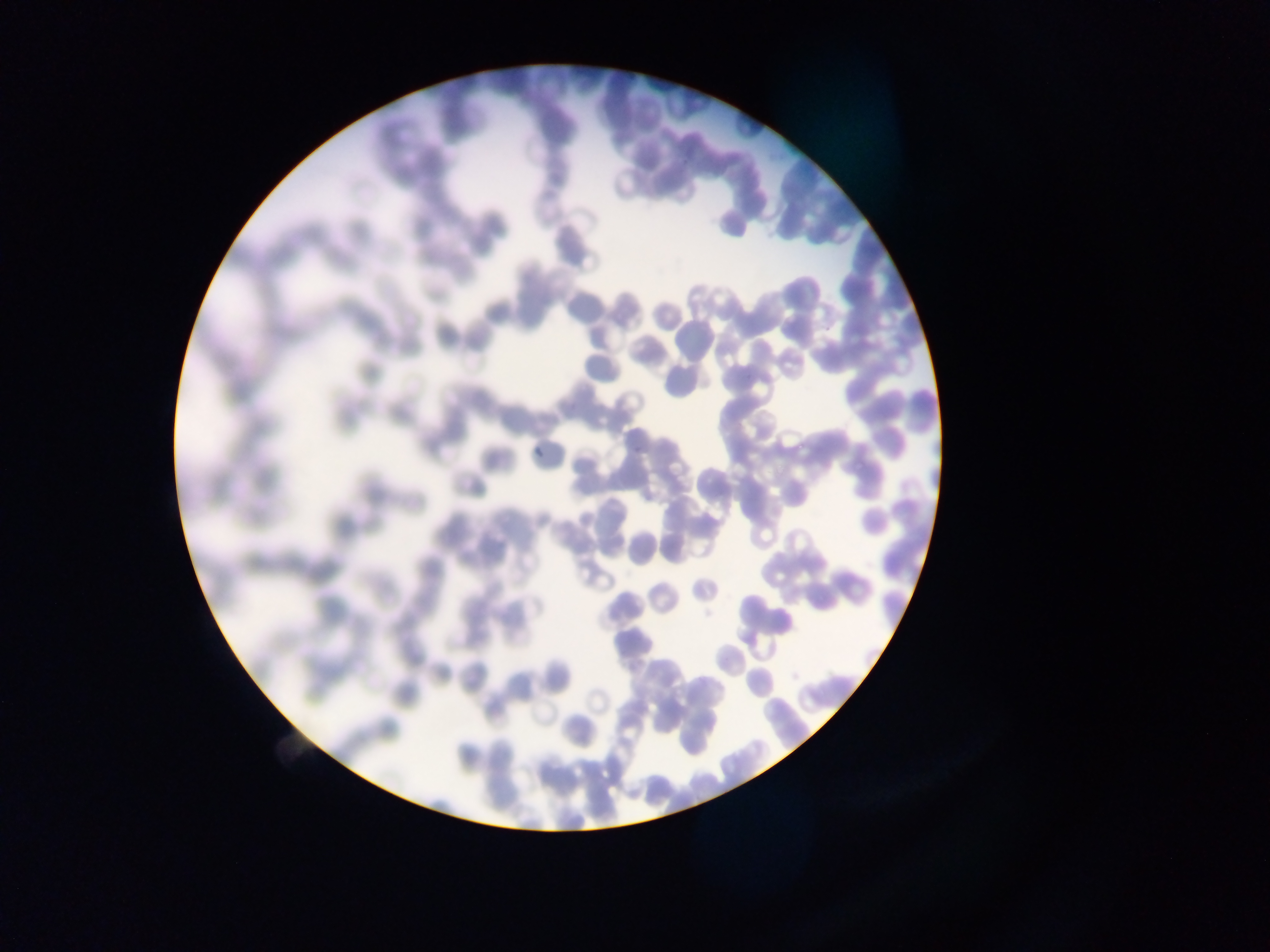
Plasmodium parasite locations = approximate bounding boxes as left top right bottom in pixels: 632 433 653 456; 532 438 553 460
preparation = thin blood film
country = Ghana
capture = mobile-phone photograph through a microscope
field of view = single
image size = 1270×952 pixels